Give the extent of all Plasmodium ovale-infected red blood cells.
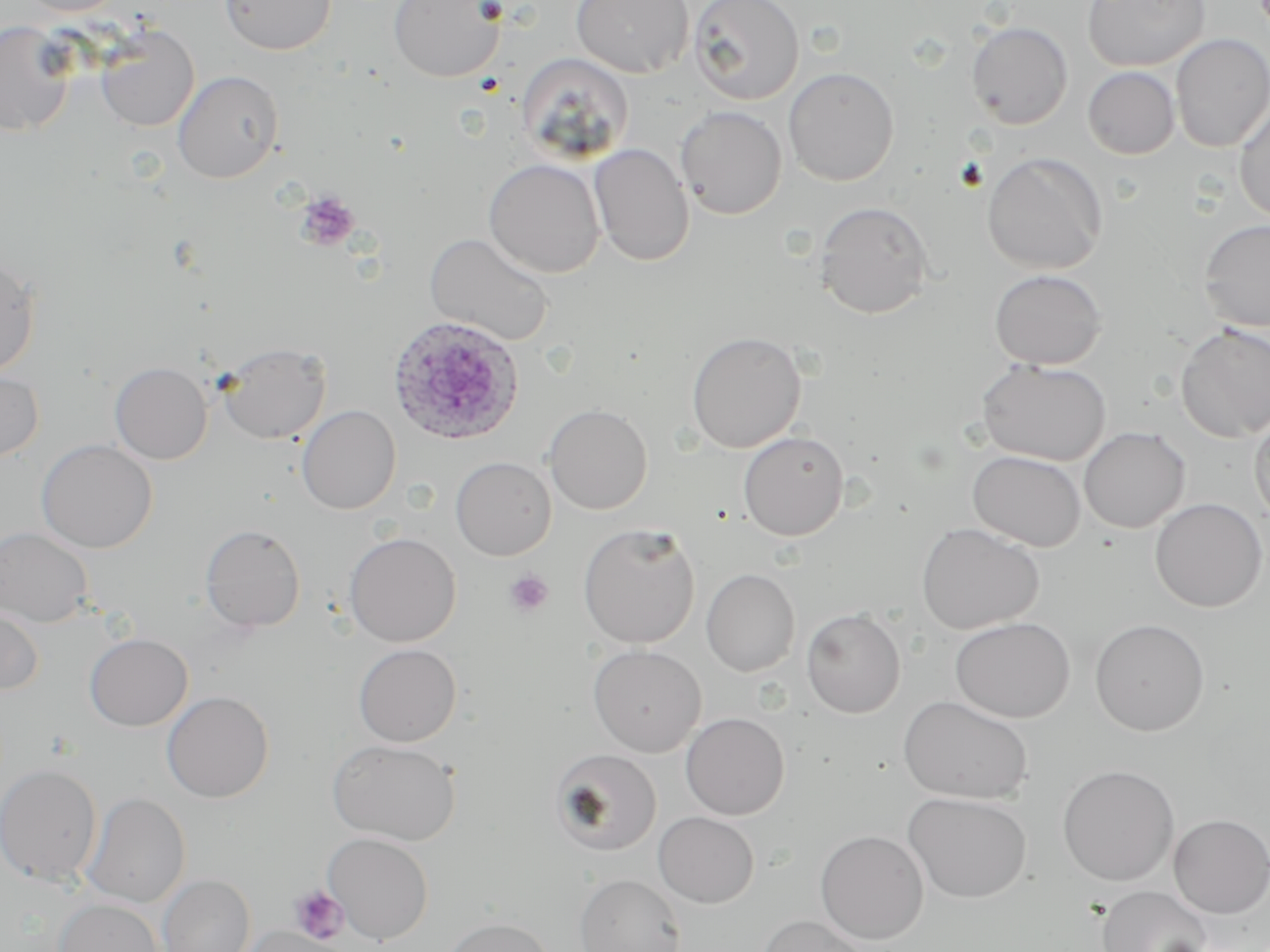
Approximate bounding boxes as named x1/y1/x2/y2 corners in pixels.
Plasmodium ovale-infected red blood cells: (x1=387, y1=315, x2=525, y2=446).

{
  "slide_level_diagnosis": "Plasmodium ovale",
  "preparation": "thin blood film",
  "field_of_view": "single",
  "image_size": "1270×952 pixels",
  "uninfected_red_blood_cell_locations": "approximate bounding boxes as named x1/y1/x2/y2 corners in pixels: (x1=17, y1=0, x2=124, y2=16), (x1=219, y1=0, x2=337, y2=55), (x1=389, y1=0, x2=506, y2=83), (x1=570, y1=0, x2=694, y2=77), (x1=688, y1=0, x2=804, y2=105), (x1=1081, y1=0, x2=1209, y2=71), (x1=0, y1=19, x2=76, y2=137), (x1=966, y1=21, x2=1073, y2=130), (x1=95, y1=25, x2=199, y2=131), (x1=1170, y1=33, x2=1270, y2=153), (x1=516, y1=52, x2=634, y2=164), (x1=783, y1=66, x2=900, y2=186), (x1=1083, y1=67, x2=1180, y2=160), (x1=173, y1=70, x2=284, y2=183), (x1=1233, y1=100, x2=1270, y2=224), (x1=675, y1=105, x2=787, y2=219), (x1=589, y1=143, x2=694, y2=266), (x1=982, y1=151, x2=1107, y2=274), (x1=484, y1=159, x2=605, y2=278), (x1=813, y1=201, x2=934, y2=319), (x1=1198, y1=218, x2=1270, y2=332), (x1=425, y1=232, x2=555, y2=347), (x1=0, y1=254, x2=41, y2=378), (x1=989, y1=269, x2=1107, y2=370), (x1=1176, y1=324, x2=1270, y2=443), (x1=686, y1=331, x2=806, y2=453), (x1=216, y1=342, x2=331, y2=444), (x1=976, y1=358, x2=1111, y2=466), (x1=110, y1=362, x2=213, y2=464), (x1=0, y1=368, x2=45, y2=463), (x1=544, y1=403, x2=653, y2=515), (x1=296, y1=405, x2=401, y2=515), (x1=1250, y1=407, x2=1270, y2=527), (x1=1078, y1=426, x2=1191, y2=533), (x1=738, y1=431, x2=849, y2=541), (x1=36, y1=439, x2=158, y2=553), (x1=967, y1=450, x2=1086, y2=551), (x1=450, y1=456, x2=556, y2=560), (x1=1149, y1=497, x2=1268, y2=612), (x1=577, y1=522, x2=701, y2=649), (x1=916, y1=522, x2=1044, y2=635), (x1=200, y1=524, x2=305, y2=633), (x1=0, y1=526, x2=95, y2=627), (x1=344, y1=532, x2=461, y2=647), (x1=701, y1=568, x2=801, y2=677), (x1=0, y1=604, x2=44, y2=695), (x1=801, y1=608, x2=906, y2=717), (x1=950, y1=616, x2=1075, y2=723), (x1=1089, y1=618, x2=1210, y2=736), (x1=85, y1=633, x2=193, y2=731), (x1=353, y1=643, x2=462, y2=747), (x1=587, y1=644, x2=707, y2=757), (x1=161, y1=690, x2=274, y2=803), (x1=898, y1=694, x2=1034, y2=804), (x1=680, y1=712, x2=790, y2=819), (x1=327, y1=738, x2=460, y2=845), (x1=550, y1=748, x2=662, y2=855), (x1=0, y1=763, x2=103, y2=885), (x1=1057, y1=764, x2=1180, y2=885), (x1=902, y1=791, x2=1032, y2=904), (x1=81, y1=793, x2=191, y2=908), (x1=653, y1=811, x2=759, y2=908), (x1=1168, y1=814, x2=1270, y2=918), (x1=815, y1=829, x2=929, y2=944), (x1=322, y1=832, x2=434, y2=944), (x1=574, y1=873, x2=686, y2=952), (x1=158, y1=874, x2=255, y2=952), (x1=1097, y1=885, x2=1212, y2=952), (x1=54, y1=899, x2=163, y2=952), (x1=758, y1=914, x2=870, y2=952), (x1=440, y1=916, x2=554, y2=952), (x1=238, y1=925, x2=347, y2=952)",
  "magnification": "1000x",
  "platelet_locations": "approximate bounding boxes as named x1/y1/x2/y2 corners in pixels: (x1=294, y1=191, x2=360, y2=252), (x1=504, y1=570, x2=553, y2=617), (x1=290, y1=886, x2=348, y2=944)",
  "modality": "optical microscopy",
  "stain": "May-Grünwald-Giemsa"
}